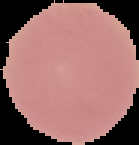
Summary:
  - Malaria status: uninfected
  - Preparation: thin blood film
  - Image type: cell region segmented out of the field of view; surrounding area masked to black
  - Image size: 139×145 pixels